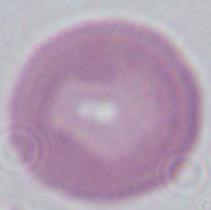
{
  "magnification": "1000x",
  "modality": "micrograph",
  "identification": "red blood cell"
}